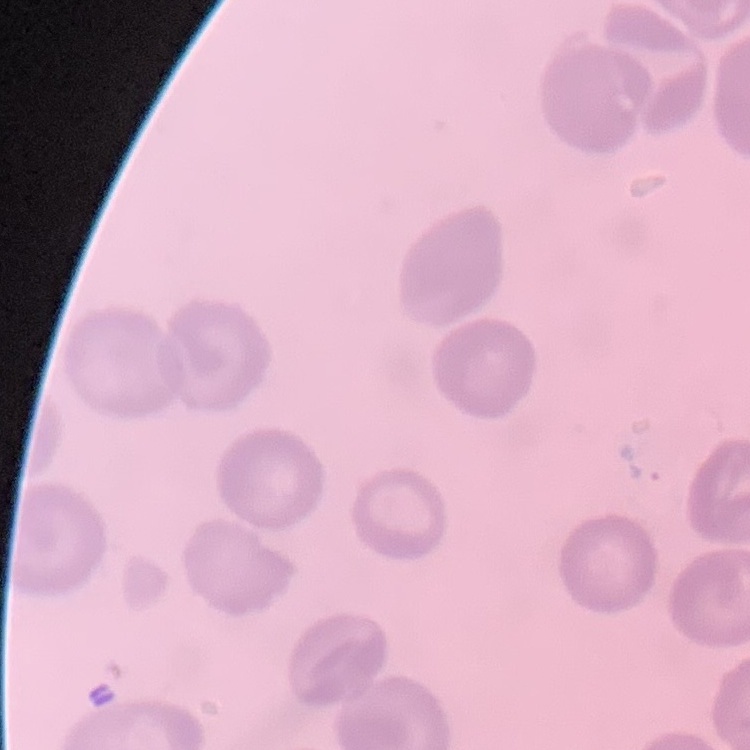

Summary:
  - Erythrocyte morphology: no rouleaux formation
  - Image type: one tile cut from a larger photomicrograph
  - Stain: Field's or Giemsa
  - Preparation: thin peripheral smear